Classify this cell by malaria status.
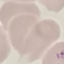

Parasitized.

Summary:
  - Stain: Giemsa
  - Image type: automatically extracted cell patch, resized to 64 × 64 pixels
  - Capture: smartphone through the microscope eyepiece
  - Preparation: thin smear